Classify this cell by malaria status.
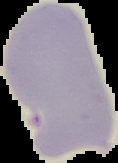
It is uninfected.

Image is 118×163 pixels. Segmented cell region on a black background. From a thin blood smear.